Identify the blood parasite species.
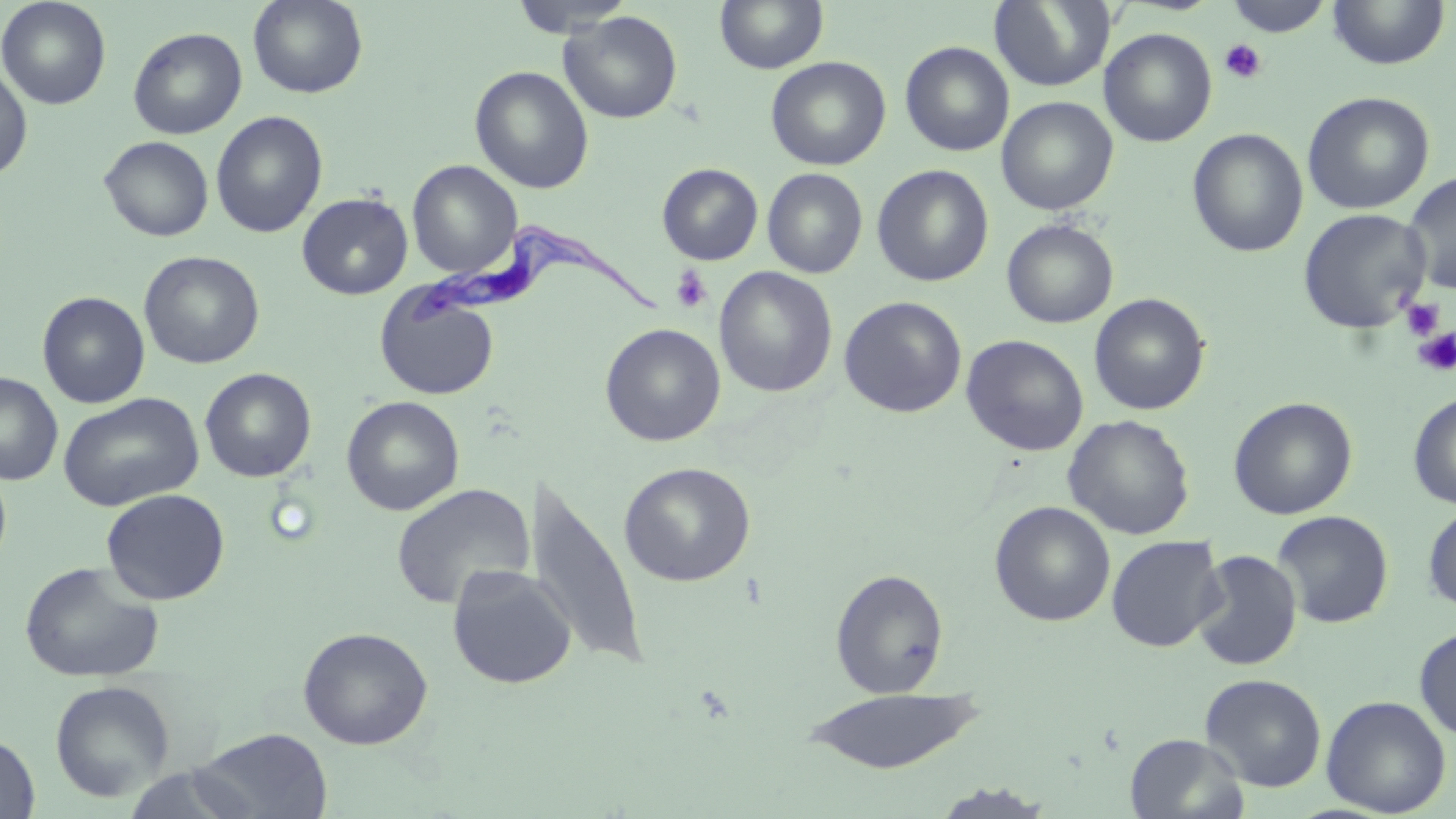
Trypanosoma brucei.

Approximate bounding boxes as (x1, y1, x2, y2) in pixels. Trypanosoma brucei locations: (401, 214, 666, 331). Uninfected red blood cell locations: (0, 0, 111, 110), (248, 0, 367, 98), (509, 0, 637, 37), (714, 0, 828, 75), (989, 0, 1115, 92), (1225, 0, 1334, 38), (1326, 0, 1451, 70), (559, 11, 682, 124), (128, 27, 247, 139), (1100, 28, 1218, 147), (900, 41, 1014, 157), (765, 56, 891, 171), (0, 64, 33, 182), (470, 65, 594, 194), (1301, 91, 1434, 214), (996, 96, 1118, 215), (210, 110, 328, 238), (1187, 128, 1309, 258), (99, 136, 214, 241), (407, 160, 522, 278), (656, 163, 763, 265), (872, 164, 994, 287), (762, 168, 868, 278), (1402, 171, 1456, 295), (297, 192, 413, 300), (1297, 208, 1431, 334), (1001, 218, 1119, 329), (139, 251, 265, 369), (714, 266, 838, 397), (375, 286, 500, 400), (37, 291, 150, 408), (1088, 292, 1210, 415), (838, 296, 968, 418), (600, 323, 726, 446), (961, 334, 1089, 456), (199, 367, 317, 482), (0, 373, 63, 485), (58, 392, 205, 511), (1408, 392, 1456, 509), (341, 395, 465, 516), (1228, 396, 1358, 520), (1063, 414, 1195, 540), (0, 460, 12, 573), (618, 462, 756, 587), (531, 471, 647, 669), (391, 482, 534, 610), (101, 488, 230, 605), (989, 501, 1115, 627), (1422, 503, 1456, 616), (1272, 510, 1394, 629), (1105, 535, 1226, 653), (1190, 549, 1303, 671), (19, 560, 164, 684), (447, 564, 576, 689), (831, 568, 948, 698), (297, 626, 433, 749), (1414, 626, 1456, 741), (1200, 673, 1327, 792), (49, 679, 175, 802), (799, 687, 985, 773), (1320, 695, 1451, 817), (192, 728, 333, 818), (1125, 733, 1249, 819), (0, 734, 39, 818), (122, 764, 259, 818), (924, 781, 1058, 818). Platelet locations: (1219, 39, 1267, 84), (669, 265, 714, 314), (1400, 299, 1444, 340), (1413, 328, 1456, 377). Image is 1456×819 pixels. Single field of view. Thin blood smear. Light microscopy. May-Grünwald-Giemsa stain. 1000x magnification.